Assess this cell for malaria.
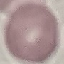
Uninfected.

Giemsa stain. Photographed with a smartphone camera at the microscope eyepiece. Automatically extracted cell patch, resized to 64 × 64 pixels. Thin smear of blood.